Identify the cell.
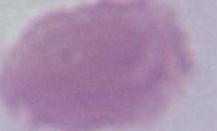
This is an erythrocyte.

1000x magnification. Micrograph.